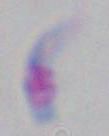

modality = micrograph
magnification = 1000x
identification = Toxoplasma gondii